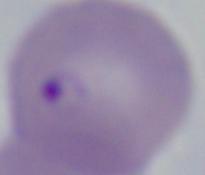

Summary:
  - Magnification: 1000x
  - Identification: Babesia
  - Modality: photomicrograph